State the blood parasite species.
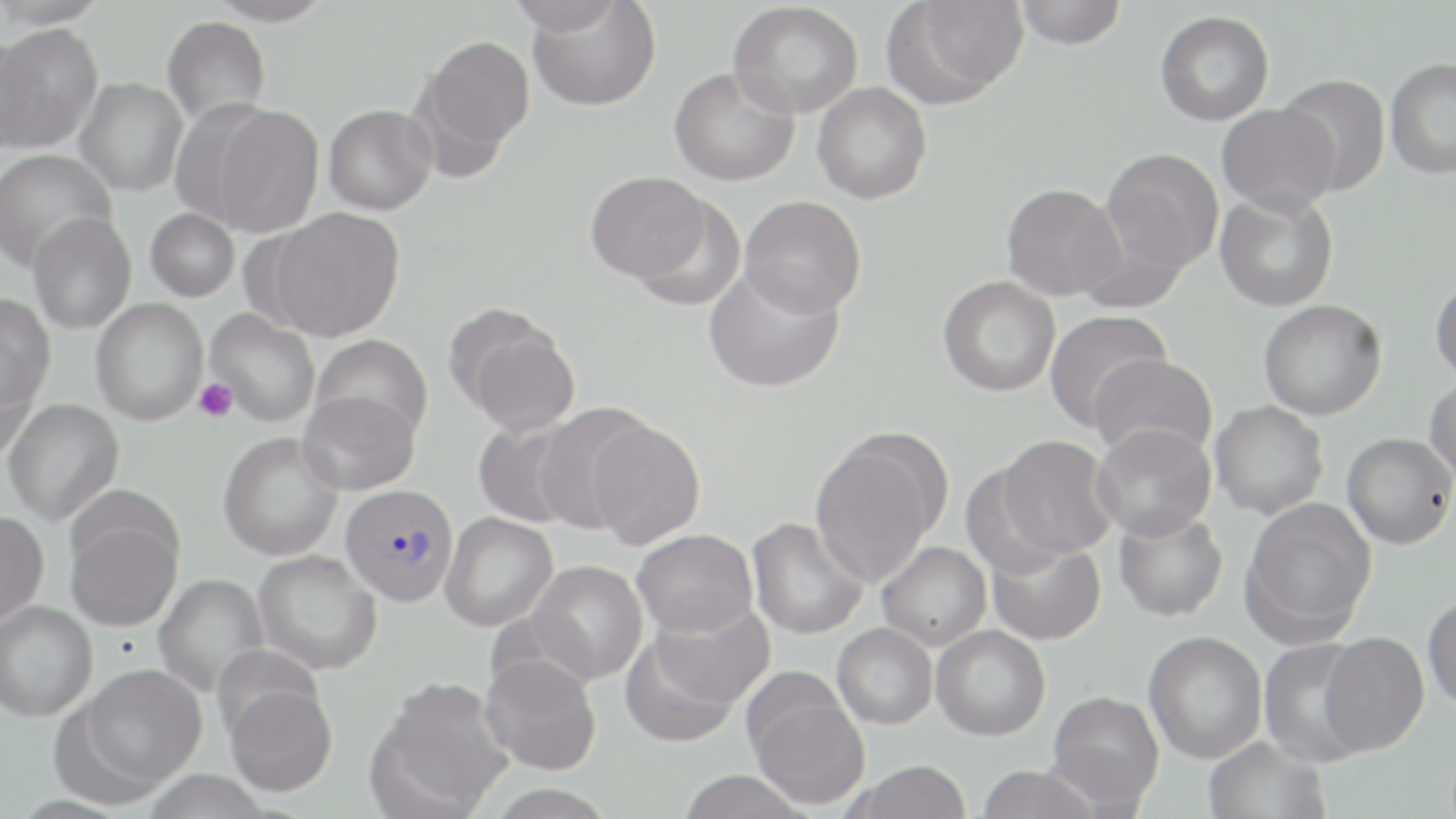

Plasmodium vivax.

Summary:
  - Coordinate format: approximate bounding boxes as named x1/y1/x2/y2 corners in pixels
  - Plasmodium vivax-infected red blood cell locations: (x1=340, y1=484, x2=458, y2=606)
  - Platelet locations: (x1=194, y1=377, x2=238, y2=423)
  - Uninfected red blood cell locations: (x1=0, y1=0, x2=109, y2=28), (x1=206, y1=0, x2=333, y2=26), (x1=505, y1=0, x2=625, y2=35), (x1=1014, y1=0, x2=1127, y2=49), (x1=527, y1=1, x2=661, y2=111), (x1=886, y1=1, x2=1026, y2=103), (x1=728, y1=2, x2=862, y2=119), (x1=1155, y1=10, x2=1275, y2=126), (x1=162, y1=16, x2=271, y2=127), (x1=1, y1=22, x2=102, y2=153), (x1=0, y1=30, x2=41, y2=155), (x1=417, y1=35, x2=535, y2=164), (x1=1385, y1=58, x2=1456, y2=181), (x1=668, y1=67, x2=799, y2=187), (x1=1278, y1=73, x2=1391, y2=196), (x1=75, y1=77, x2=187, y2=197), (x1=812, y1=82, x2=932, y2=204), (x1=207, y1=103, x2=325, y2=237), (x1=1217, y1=103, x2=1341, y2=218), (x1=323, y1=104, x2=437, y2=216), (x1=0, y1=148, x2=117, y2=273), (x1=1100, y1=148, x2=1224, y2=274), (x1=585, y1=171, x2=716, y2=283), (x1=1001, y1=183, x2=1125, y2=301), (x1=1215, y1=189, x2=1339, y2=312), (x1=628, y1=194, x2=746, y2=311), (x1=740, y1=195, x2=866, y2=318), (x1=145, y1=208, x2=239, y2=302), (x1=266, y1=208, x2=405, y2=342), (x1=28, y1=212, x2=136, y2=334), (x1=703, y1=265, x2=844, y2=393), (x1=938, y1=275, x2=1060, y2=397), (x1=1430, y1=277, x2=1456, y2=386), (x1=0, y1=294, x2=56, y2=409), (x1=91, y1=298, x2=208, y2=425), (x1=1257, y1=299, x2=1386, y2=421), (x1=205, y1=309, x2=320, y2=425), (x1=1044, y1=309, x2=1170, y2=435), (x1=452, y1=310, x2=580, y2=436), (x1=311, y1=335, x2=433, y2=442), (x1=1089, y1=354, x2=1217, y2=461), (x1=0, y1=358, x2=37, y2=461), (x1=1425, y1=374, x2=1456, y2=487), (x1=297, y1=391, x2=419, y2=496), (x1=2, y1=398, x2=124, y2=526), (x1=1209, y1=401, x2=1329, y2=520), (x1=535, y1=403, x2=655, y2=533), (x1=473, y1=419, x2=584, y2=528), (x1=586, y1=419, x2=706, y2=549), (x1=1091, y1=422, x2=1216, y2=541), (x1=218, y1=432, x2=343, y2=561), (x1=1342, y1=432, x2=1455, y2=549), (x1=809, y1=435, x2=944, y2=587), (x1=994, y1=435, x2=1118, y2=558), (x1=960, y1=460, x2=1076, y2=575), (x1=1241, y1=497, x2=1377, y2=640), (x1=0, y1=509, x2=49, y2=627), (x1=1113, y1=509, x2=1228, y2=622), (x1=440, y1=512, x2=558, y2=632), (x1=65, y1=515, x2=182, y2=632), (x1=747, y1=517, x2=870, y2=640), (x1=632, y1=529, x2=757, y2=637), (x1=985, y1=537, x2=1106, y2=645), (x1=877, y1=541, x2=992, y2=651), (x1=253, y1=549, x2=383, y2=675), (x1=526, y1=560, x2=648, y2=685), (x1=154, y1=573, x2=269, y2=698), (x1=1422, y1=594, x2=1456, y2=712), (x1=644, y1=598, x2=775, y2=712), (x1=0, y1=601, x2=97, y2=721), (x1=832, y1=623, x2=938, y2=729), (x1=931, y1=624, x2=1051, y2=741), (x1=620, y1=629, x2=744, y2=749), (x1=1144, y1=631, x2=1268, y2=763), (x1=1319, y1=632, x2=1429, y2=755), (x1=1257, y1=638, x2=1373, y2=767), (x1=480, y1=652, x2=602, y2=775), (x1=78, y1=664, x2=207, y2=790), (x1=371, y1=676, x2=514, y2=817), (x1=224, y1=681, x2=338, y2=797), (x1=746, y1=685, x2=870, y2=810), (x1=1047, y1=691, x2=1164, y2=810), (x1=1203, y1=736, x2=1331, y2=819), (x1=848, y1=760, x2=972, y2=819), (x1=976, y1=765, x2=1101, y2=819), (x1=676, y1=770, x2=811, y2=819)
  - Modality: optical microscopy
  - Stain: May-Grünwald-Giemsa
  - Magnification: 1000x
  - Preparation: thin blood film
  - Image size: 1456×819 pixels
  - Field of view: one of a larger specimen